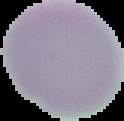

Summary:
  - Malaria status: uninfected
  - Image type: cell region segmented out of the field of view; surrounding area masked to black
  - Image size: 124×121 pixels
  - Preparation: thin blood smear